Locate every Plasmodium falciparum-infected red blood cell.
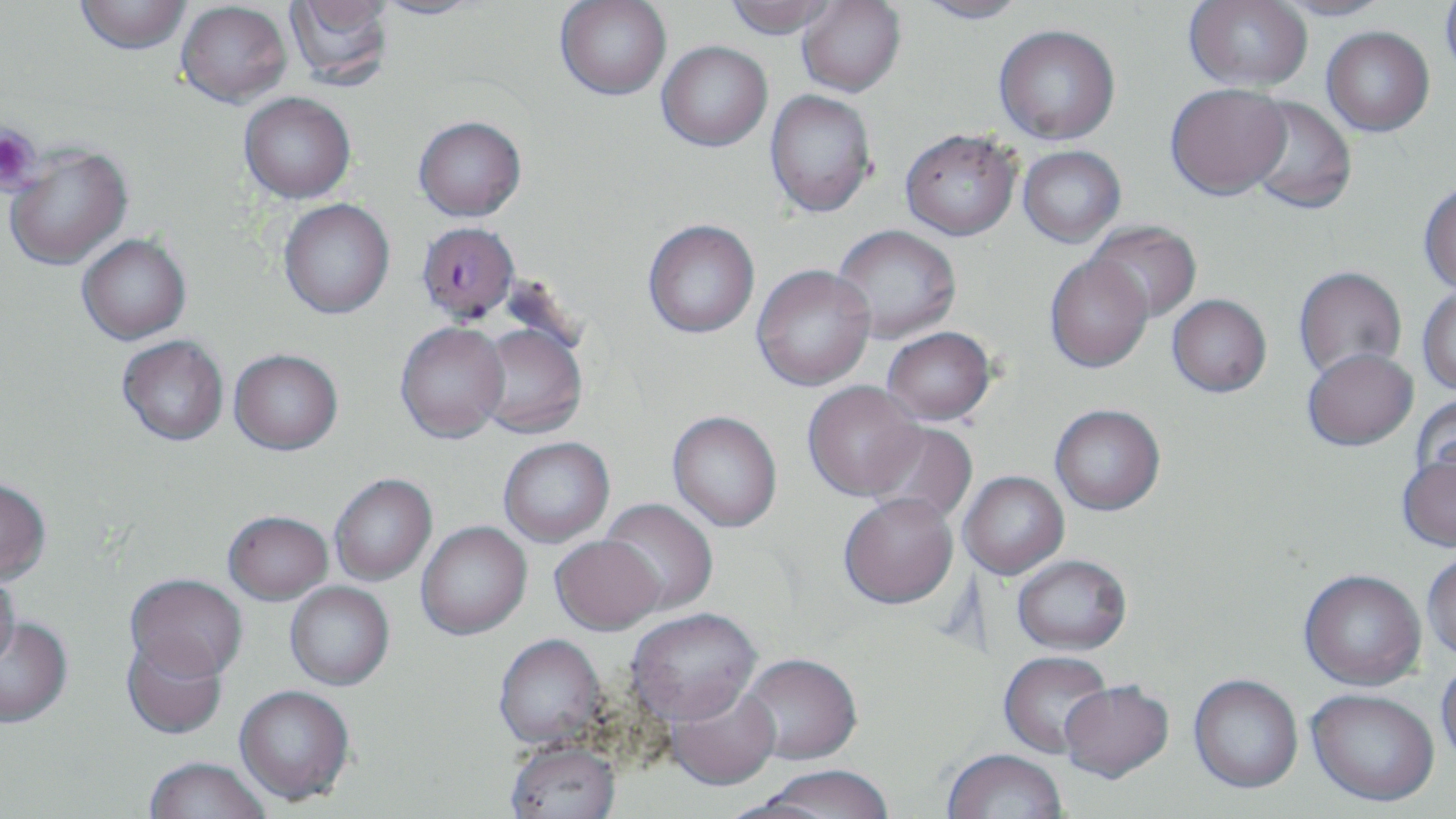

Approximate bounding boxes as [x1, y1, x2, y2] in pixels.
Plasmodium falciparum-infected red blood cells: [417, 223, 519, 324].

Platelet locations: [0, 123, 42, 194]. Uninfected red blood cell locations: [75, 0, 192, 54], [283, 0, 394, 88], [369, 0, 486, 20], [555, 0, 671, 100], [723, 0, 840, 39], [915, 0, 1030, 25], [176, 1, 291, 107], [797, 1, 906, 97], [1184, 1, 1313, 89], [1271, 1, 1394, 21], [1440, 1, 1456, 82], [994, 24, 1120, 145], [1322, 26, 1434, 136], [657, 41, 772, 152], [1165, 83, 1291, 200], [764, 90, 877, 218], [240, 92, 356, 203], [1244, 96, 1356, 215], [413, 116, 526, 221], [900, 128, 1021, 241], [4, 144, 133, 272], [1018, 146, 1125, 247], [1418, 182, 1456, 294], [278, 199, 395, 319], [642, 219, 760, 339], [1087, 221, 1202, 322], [832, 224, 962, 342], [78, 235, 191, 344], [1044, 254, 1153, 373], [751, 264, 876, 391], [1293, 267, 1407, 381], [1417, 285, 1456, 396], [1167, 294, 1271, 397], [395, 323, 509, 445], [474, 324, 588, 439], [882, 327, 995, 425], [117, 336, 229, 447], [1302, 348, 1418, 450], [229, 351, 343, 457], [803, 381, 925, 502], [1412, 395, 1456, 490], [1050, 404, 1165, 515], [667, 413, 783, 533], [864, 421, 978, 527], [498, 438, 615, 548], [1396, 453, 1456, 552], [959, 472, 1069, 580], [330, 475, 437, 586], [0, 481, 51, 587], [839, 495, 958, 611], [599, 498, 718, 616], [224, 513, 334, 607], [416, 523, 532, 641], [550, 538, 665, 638], [1422, 551, 1456, 661], [1012, 555, 1132, 656], [1298, 570, 1426, 692], [0, 572, 20, 671], [125, 576, 248, 685], [284, 582, 394, 691], [626, 610, 761, 730], [0, 619, 73, 730], [494, 636, 607, 752], [121, 638, 227, 740], [999, 653, 1113, 760], [739, 656, 862, 768], [1436, 659, 1456, 768], [1188, 676, 1303, 796], [664, 684, 782, 793], [1060, 684, 1174, 787], [234, 687, 354, 808], [1306, 691, 1438, 809], [505, 744, 621, 819], [942, 751, 1067, 819], [143, 759, 271, 818], [760, 769, 895, 819]. Slide-level diagnosis: Plasmodium falciparum. Image is 1456×819 pixels. Light microscopy. May-Grünwald-Giemsa-stained preparation. One field of a larger specimen. Thin blood smear. 1000x magnification.